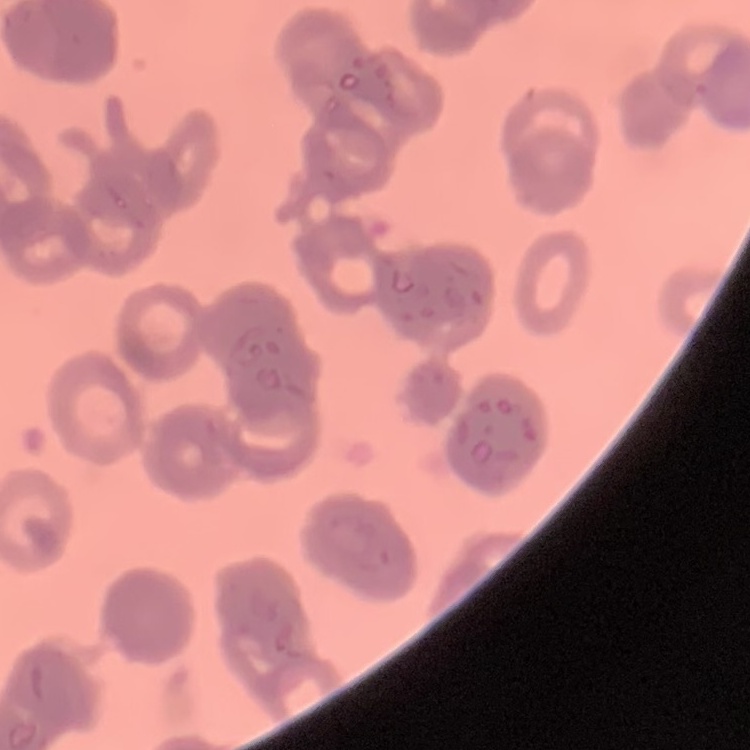
red blood cell morphology = rouleaux formation
image type = one tile cut from a larger photomicrograph
preparation = thin blood film
stain = Field's or Giemsa